State which parasite is depicted.
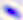
Toxoplasma gondii.

magnification = 400x
modality = micrograph